State the blood parasite species.
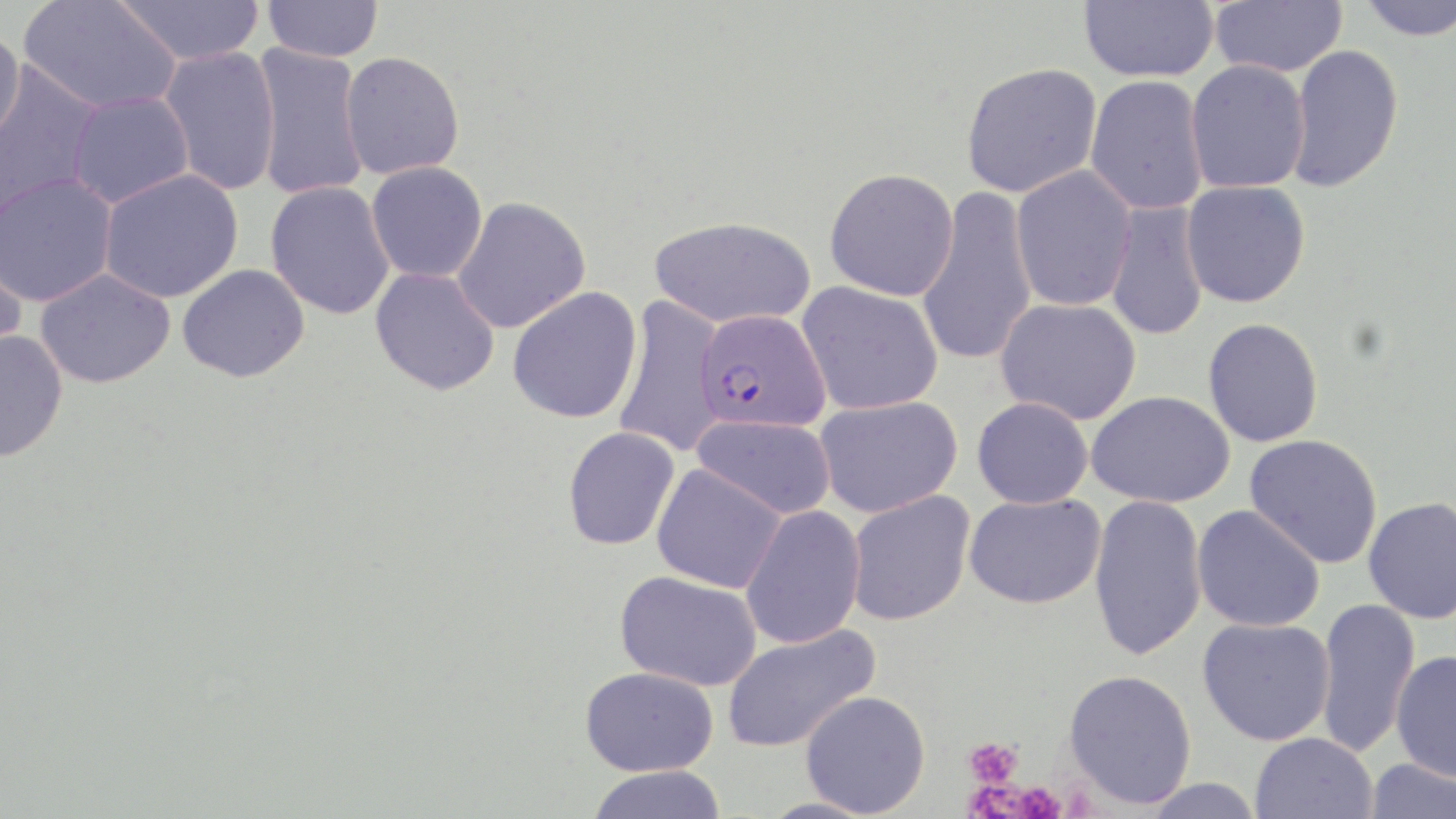

Plasmodium falciparum.

Approximate bounding boxes as (x1, y1, x2, y2) in pixels. Uninfected red blood cell locations: (18, 0, 181, 115), (113, 0, 266, 67), (263, 0, 383, 62), (1080, 0, 1219, 83), (1210, 0, 1347, 77), (1356, 0, 1456, 41), (0, 24, 25, 148), (1287, 44, 1404, 193), (251, 45, 369, 201), (159, 46, 281, 197), (339, 51, 465, 179), (1186, 60, 1310, 194), (961, 62, 1103, 197), (0, 64, 106, 222), (1085, 75, 1209, 215), (68, 92, 193, 207), (366, 161, 487, 283), (1010, 165, 1136, 311), (824, 168, 959, 301), (98, 169, 243, 303), (0, 172, 117, 307), (1181, 180, 1310, 307), (265, 181, 395, 319), (915, 187, 1039, 368), (452, 196, 591, 334), (1105, 201, 1209, 342), (649, 216, 814, 328), (0, 238, 27, 363), (177, 263, 310, 382), (370, 267, 500, 395), (34, 268, 175, 388), (796, 281, 943, 415), (508, 286, 643, 424), (613, 296, 727, 458), (996, 298, 1141, 424), (1203, 318, 1323, 447), (0, 327, 68, 463), (1087, 390, 1235, 508), (815, 396, 962, 518), (972, 397, 1094, 509), (693, 415, 835, 519), (562, 426, 680, 551), (1244, 434, 1383, 569), (651, 463, 786, 593), (847, 491, 975, 626), (965, 493, 1105, 609), (1089, 494, 1207, 661), (1364, 497, 1456, 624), (740, 505, 866, 649), (1193, 505, 1325, 632), (614, 570, 761, 691), (1316, 598, 1420, 758), (1198, 617, 1336, 745), (722, 622, 879, 752), (1390, 649, 1456, 782), (580, 666, 718, 776), (1064, 668, 1197, 809), (800, 690, 931, 817), (1250, 732, 1377, 819), (1364, 757, 1455, 818), (586, 765, 728, 819), (1137, 778, 1268, 818). Plasmodium falciparum-infected red blood cell locations: (695, 309, 831, 433). Platelet locations: (964, 736, 1023, 788), (969, 780, 1022, 818), (1012, 781, 1066, 819). Light microscopy. Thin blood film. May-Grünwald-Giemsa-stained preparation. One field of a larger specimen. 1000x magnification. Image is 1456×819 pixels.